Classify this cell by malaria status.
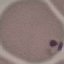

It is parasitized.

stain = Giemsa
capture = smartphone camera at the microscope eyepiece
preparation = thin blood film
image type = cell patch, automatically extracted from a larger field of view and resized to 64 × 64 pixels